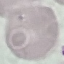
Malaria status: uninfected. Giemsa-stained preparation. Automatically extracted cell patch, resized to 64 × 64 pixels. Photographed with a smartphone camera at the microscope eyepiece. Thin blood smear.